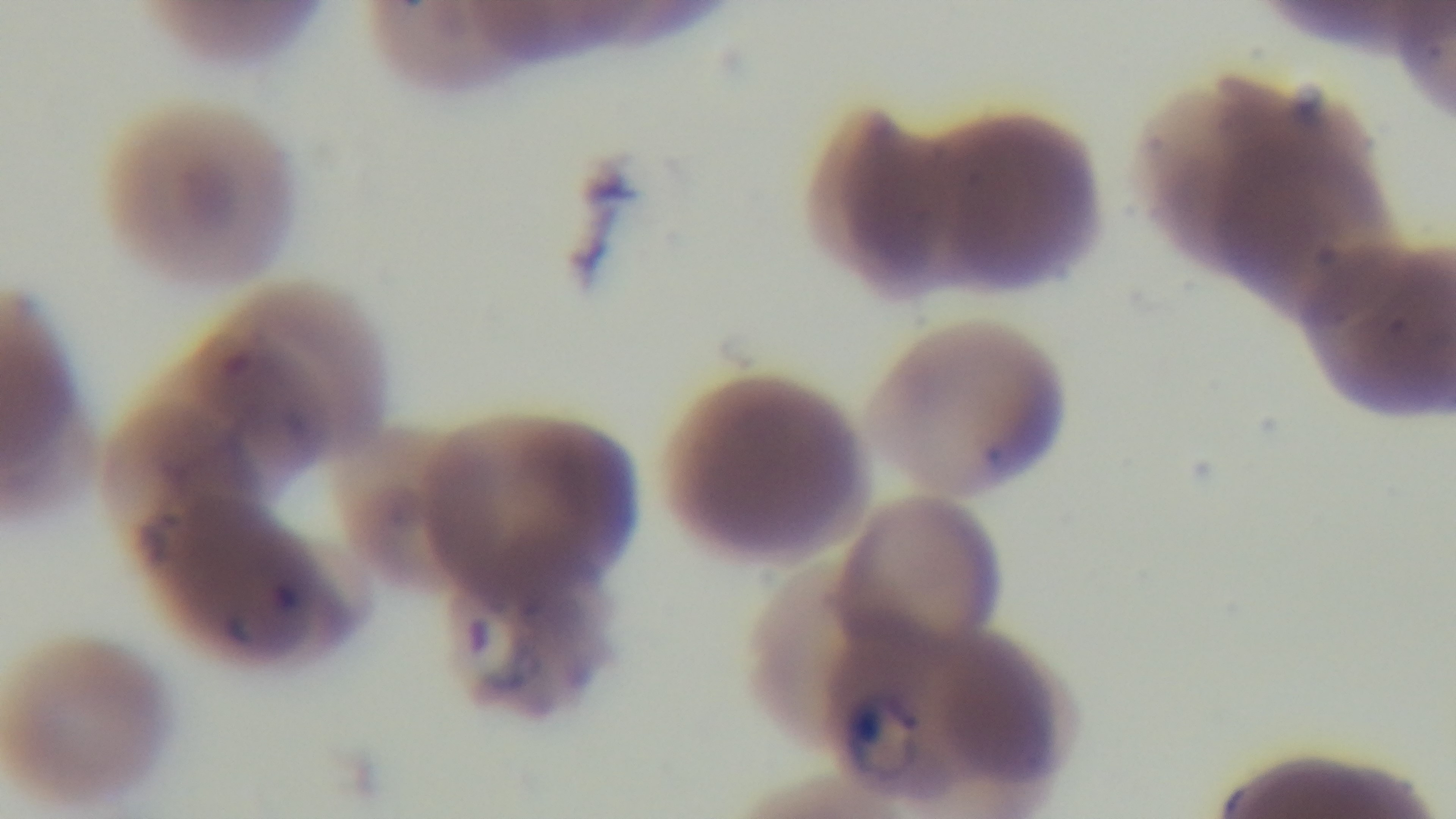
Summary:
  - Modality: light microscopy
  - Stain: Giemsa
  - Preparation: thin blood film
  - Objective: 100x oil immersion
  - Malaria status: infected
  - Capture: mounted 4K digital camera
  - Field of view: one from the slide